Mark where platelets are.
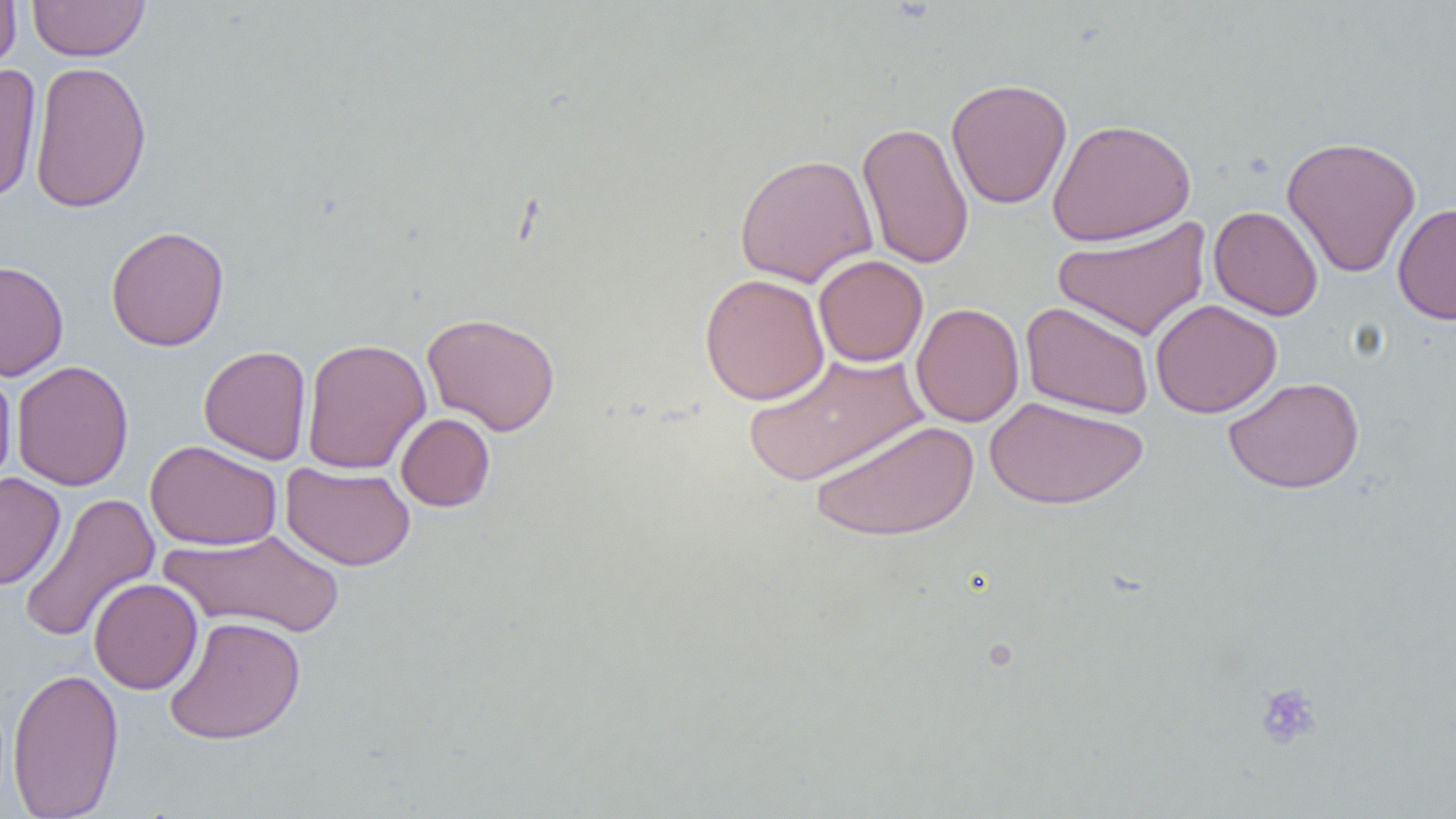

Approximate bounding boxes as (x1,y1)-(x2,y2) corner pairs in pixels.
Platelets: (1255,682)-(1322,749).

slide-level diagnosis = no evidence of blood parasites
field of view = one of a larger specimen
magnification = 1000x
image size = 1456×819 pixels
preparation = thin blood smear
modality = light microscopy
uninfected red blood cell locations = approximate bounding boxes as (x1,y1)-(x2,y2) corner pairs in pixels: (0,0)-(20,81), (27,1)-(149,61), (29,60)-(152,214), (0,64)-(42,205), (946,77)-(1073,209), (1047,118)-(1196,246), (856,121)-(974,270), (1281,135)-(1421,278), (734,153)-(878,288), (1392,202)-(1456,325), (1208,205)-(1323,321), (1052,217)-(1212,342), (105,225)-(230,351), (813,254)-(928,367), (0,259)-(68,381), (700,273)-(829,405), (1150,298)-(1283,418), (1020,301)-(1154,420), (911,302)-(1024,428), (422,311)-(561,435), (301,338)-(431,475), (198,345)-(312,464), (742,350)-(929,487), (11,360)-(134,491), (0,361)-(16,493), (1223,376)-(1365,494), (984,395)-(1148,510), (395,413)-(495,512), (809,418)-(980,542), (145,440)-(282,551), (280,461)-(415,570), (0,472)-(66,590), (17,493)-(160,644), (160,529)-(346,638), (88,577)-(203,695), (163,615)-(306,745), (6,666)-(124,819)